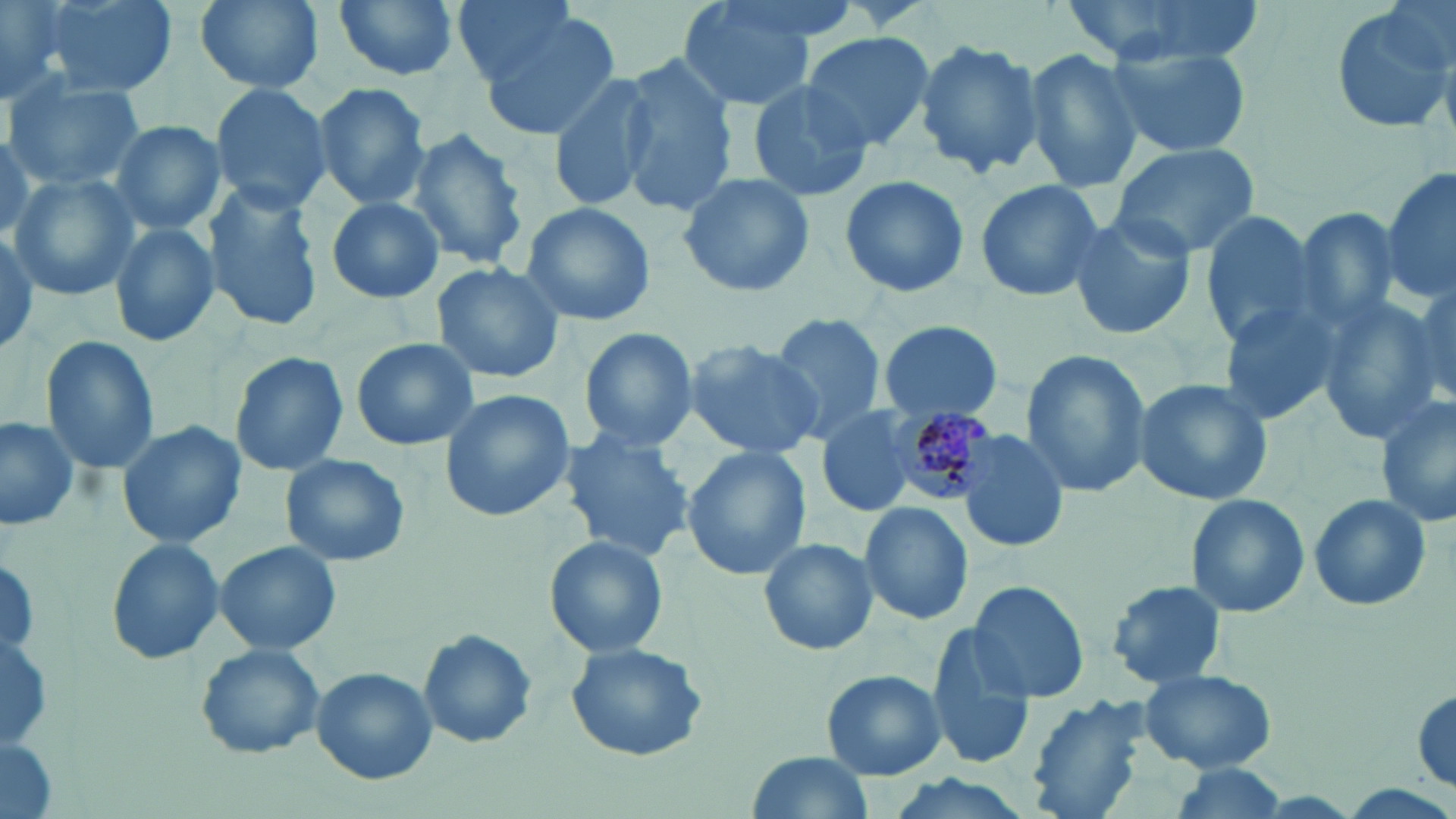
slide-level diagnosis = Plasmodium malariae
preparation = thin blood smear
uninfected red blood cell locations = approximate bounding boxes as (x1,y1)-(x2,y2) corner pairs in pixels: (0,0)-(72,101), (42,0)-(177,97), (191,0)-(329,95), (332,0)-(462,85), (449,0)-(581,88), (675,0)-(819,112), (1065,0)-(1257,62), (1330,0)-(1453,136), (472,10)-(622,143), (798,31)-(936,153), (914,38)-(1045,179), (1108,43)-(1252,159), (1022,49)-(1143,194), (618,58)-(736,216), (548,72)-(660,212), (5,74)-(147,192), (746,80)-(876,202), (210,82)-(334,214), (313,82)-(432,211), (108,119)-(226,237), (406,129)-(529,270), (1110,142)-(1260,258), (1383,163)-(1456,309), (677,171)-(815,298), (839,173)-(970,298), (8,174)-(138,299), (974,178)-(1104,302), (203,183)-(326,330), (326,196)-(445,304), (518,202)-(657,325), (1289,205)-(1405,338), (1063,211)-(1197,341), (1198,213)-(1322,348), (109,222)-(222,349), (0,227)-(51,351), (430,261)-(566,384), (1406,277)-(1454,406), (1316,293)-(1447,440), (1215,298)-(1343,427), (767,314)-(886,439), (872,320)-(1003,424), (576,327)-(699,453), (40,336)-(161,474), (350,338)-(480,452), (681,338)-(824,458), (1018,348)-(1152,498), (228,350)-(352,477), (1131,378)-(1274,506), (438,387)-(574,521), (1375,394)-(1455,530), (812,406)-(920,519), (0,415)-(83,533), (116,420)-(247,550), (956,427)-(1069,555), (558,430)-(697,563), (1345,437)-(1445,582), (680,447)-(810,581), (280,453)-(410,568), (1185,493)-(1310,616), (1307,494)-(1432,612), (859,500)-(976,626), (544,536)-(670,661), (106,537)-(227,665), (758,537)-(878,657), (214,541)-(343,656), (1104,579)-(1229,690), (967,580)-(1089,703), (925,626)-(1036,769), (1,627)-(55,749), (418,629)-(537,749), (565,641)-(709,761), (194,645)-(326,761), (311,667)-(437,786), (821,669)-(946,781), (1139,669)-(1275,773), (1411,686)-(1454,796), (1022,695)-(1152,819), (0,734)-(59,819), (748,752)-(873,819), (1169,763)-(1288,817), (876,771)-(1038,819)
stain = May-Grünwald-Giemsa
field of view = single
magnification = 1000x
image size = 1456×819 pixels
modality = light microscopy
Plasmodium malariae-infected red blood cell locations = approximate bounding boxes as (x1,y1)-(x2,y2) corner pairs in pixels: (889,406)-(997,503)